Assess this cell for malaria.
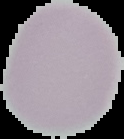
It is uninfected.

{
  "image_type": "segmented cell region with the area outside set to black",
  "preparation": "thin blood smear",
  "image_size": "124×139 pixels"
}